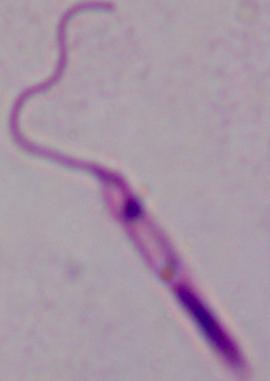

Summary:
  - Identification: Leishmania
  - Modality: micrograph
  - Magnification: 1000x